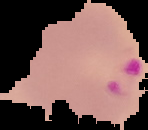
Malaria status: parasitized. Segmented cell region on a black background. Image is 148×130 pixels. From a thin blood smear.